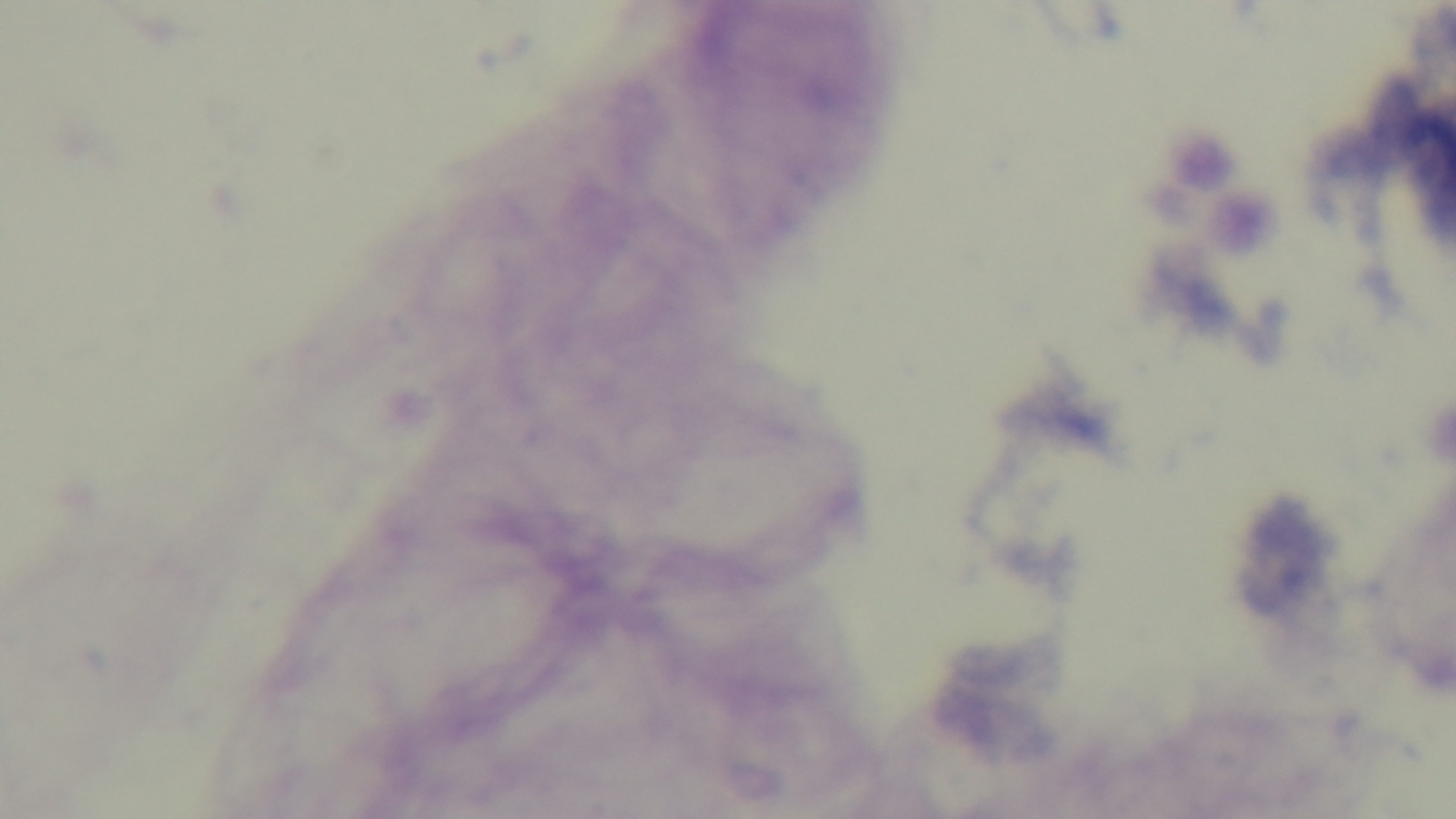

Light microscopy. Malaria status: negative. 100x oil-immersion objective. Mounted 4K digital camera. One field from the slide. Giemsa-stained. Preparation: thick blood film.